Outline each Trypanosoma brucei.
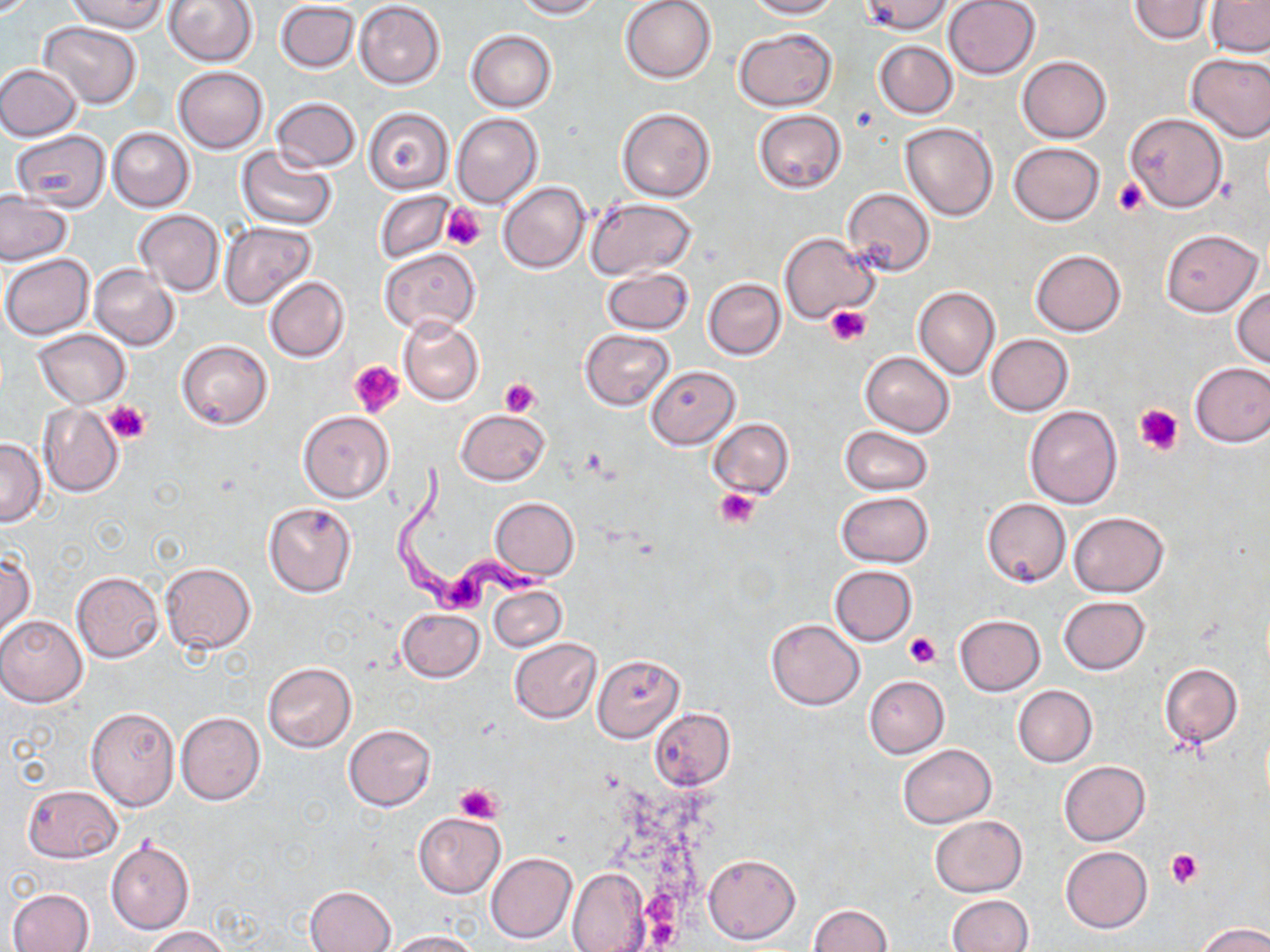
Approximate bounding boxes as (x1, y1, x2, y2) in pixels.
Trypanosoma brucei: (392, 459, 555, 613).

Uninfected red blood cell locations: (65, 0, 169, 33), (163, 0, 258, 68), (513, 0, 604, 18), (621, 0, 717, 83), (746, 0, 839, 18), (861, 0, 954, 34), (943, 0, 1041, 80), (1128, 0, 1214, 44), (354, 1, 445, 89), (1206, 1, 1270, 57), (275, 2, 359, 72), (39, 22, 141, 108), (733, 28, 838, 111), (466, 30, 557, 112), (874, 40, 958, 118), (1185, 53, 1270, 142), (1018, 56, 1111, 143), (0, 63, 82, 140), (173, 66, 268, 153), (270, 98, 360, 172), (363, 108, 453, 193), (616, 108, 714, 201), (753, 109, 847, 194), (452, 113, 543, 210), (1124, 113, 1228, 212), (900, 121, 998, 220), (107, 128, 195, 211), (11, 129, 111, 211), (1008, 142, 1105, 226), (236, 145, 338, 230), (497, 181, 591, 273), (842, 188, 935, 277), (0, 189, 74, 266), (375, 190, 455, 264), (585, 198, 699, 280), (134, 209, 225, 295), (218, 221, 316, 310), (1161, 229, 1262, 316), (779, 232, 878, 326), (380, 248, 480, 335), (1030, 248, 1126, 336), (2, 255, 94, 339), (89, 265, 180, 350), (601, 267, 695, 335), (264, 277, 349, 362), (703, 277, 786, 359), (1231, 286, 1269, 368), (913, 287, 1000, 380), (398, 317, 483, 405), (33, 329, 130, 408), (581, 329, 675, 409), (984, 335, 1073, 416), (177, 339, 273, 430), (861, 351, 954, 436), (1190, 361, 1270, 447), (645, 366, 740, 450), (38, 404, 124, 497), (1025, 404, 1123, 508), (455, 410, 550, 485), (298, 411, 392, 501), (707, 418, 794, 499), (840, 425, 932, 495), (0, 438, 46, 526), (835, 492, 934, 567), (489, 497, 580, 581), (982, 498, 1070, 587), (263, 501, 358, 598), (1068, 512, 1168, 597), (1, 549, 35, 641), (160, 562, 257, 653), (829, 565, 916, 645), (71, 571, 163, 661), (487, 582, 566, 652), (1058, 596, 1151, 674), (397, 609, 484, 682), (954, 615, 1046, 696), (0, 616, 88, 706), (766, 619, 864, 709), (509, 637, 602, 724), (592, 655, 686, 742), (262, 661, 357, 753), (1159, 663, 1244, 749), (864, 675, 948, 758), (1012, 685, 1097, 767), (86, 707, 179, 810), (649, 708, 734, 790), (175, 712, 264, 805), (344, 723, 436, 811), (897, 744, 996, 828), (1059, 761, 1150, 846), (22, 785, 122, 862), (414, 813, 505, 897), (930, 814, 1027, 897), (106, 840, 194, 934), (1060, 846, 1153, 932), (485, 851, 577, 944), (703, 853, 800, 945), (565, 867, 653, 951), (305, 885, 397, 951), (7, 888, 94, 952), (947, 895, 1033, 952), (807, 905, 892, 952), (1194, 922, 1270, 952), (142, 926, 232, 951), (384, 930, 480, 952). Platelet locations: (1113, 178, 1149, 215), (440, 206, 485, 249), (826, 306, 871, 346), (349, 360, 404, 419), (500, 378, 541, 417), (104, 400, 152, 443), (1134, 403, 1184, 456), (715, 487, 760, 529), (905, 630, 939, 668), (455, 783, 505, 823), (1168, 849, 1204, 888). Slide-level diagnosis: Trypanosoma brucei. Light microscopy. Image is 1270×952 pixels. One field of a larger specimen. May-Grünwald-Giemsa-stained preparation. Captured at 1000x magnification. Thin blood film.